Name the blood parasite species.
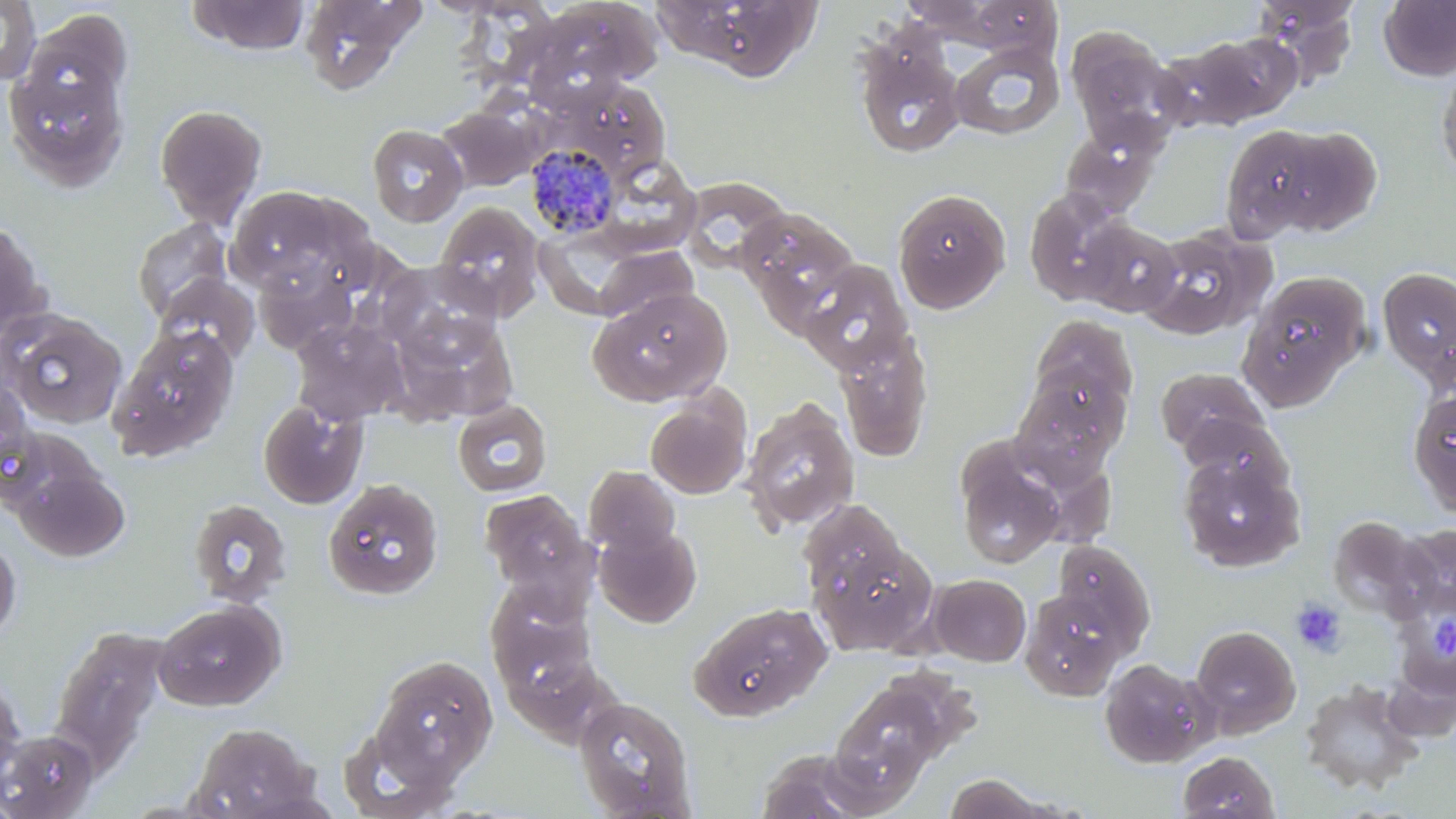
Plasmodium malariae.

Approximate bounding boxes as [x1, y1, x2, y2] in pixels. Plasmodium malariae-infected red blood cell locations: [525, 142, 622, 239]. Uninfected red blood cell locations: [0, 0, 41, 86], [186, 0, 311, 56], [299, 0, 423, 95], [525, 0, 663, 104], [653, 0, 795, 90], [1253, 0, 1361, 86], [1378, 0, 1456, 81], [23, 9, 132, 111], [1065, 26, 1182, 144], [1199, 32, 1305, 124], [854, 36, 966, 160], [949, 41, 1066, 140], [2, 58, 130, 192], [1437, 60, 1456, 182], [569, 78, 670, 177], [436, 102, 542, 191], [154, 103, 268, 226], [1219, 122, 1352, 243], [366, 123, 468, 227], [1060, 125, 1163, 218], [682, 176, 791, 275], [225, 185, 361, 297], [891, 187, 1012, 313], [1024, 187, 1130, 306], [435, 202, 546, 320], [738, 207, 861, 324], [132, 218, 233, 322], [1076, 218, 1183, 317], [0, 219, 50, 339], [1137, 227, 1271, 339], [528, 233, 664, 314], [594, 246, 699, 327], [376, 259, 508, 362], [253, 262, 357, 354], [802, 262, 915, 376], [1377, 266, 1456, 386], [1237, 271, 1370, 407], [155, 275, 259, 365], [588, 286, 733, 408], [1, 308, 126, 429], [1029, 315, 1138, 421], [291, 319, 408, 425], [107, 325, 240, 461], [836, 331, 934, 462], [1156, 367, 1267, 458], [1010, 375, 1127, 489], [1407, 387, 1456, 516], [644, 391, 752, 500], [740, 397, 860, 533], [257, 399, 367, 509], [452, 400, 552, 497], [1180, 413, 1294, 501], [954, 448, 1065, 570], [1177, 455, 1304, 572], [12, 463, 130, 562], [584, 465, 680, 556], [324, 477, 445, 597], [479, 490, 592, 598], [187, 498, 292, 607], [797, 500, 909, 610], [1329, 514, 1428, 615], [1398, 523, 1456, 615], [594, 524, 702, 627], [0, 533, 21, 646], [810, 534, 937, 654], [1050, 539, 1156, 652], [929, 573, 1031, 666], [485, 583, 595, 689], [1393, 584, 1456, 711], [1019, 586, 1130, 700], [152, 599, 285, 711], [689, 602, 832, 721], [1190, 624, 1301, 736], [49, 627, 169, 769], [370, 654, 498, 782], [503, 654, 617, 748], [1098, 657, 1214, 768], [0, 674, 26, 782], [829, 680, 944, 798], [1299, 681, 1423, 793], [573, 696, 697, 817], [188, 721, 321, 818], [338, 723, 461, 817], [1, 729, 99, 818], [752, 750, 881, 819], [1176, 750, 1281, 818], [941, 773, 1059, 818]. Platelet locations: [1291, 597, 1347, 658], [1429, 607, 1456, 659]. Captured at 1000x magnification. One field of a larger specimen. Image is 1456×819 pixels. Light microscopy. May-Grünwald-Giemsa-stained preparation. Thin blood smear.